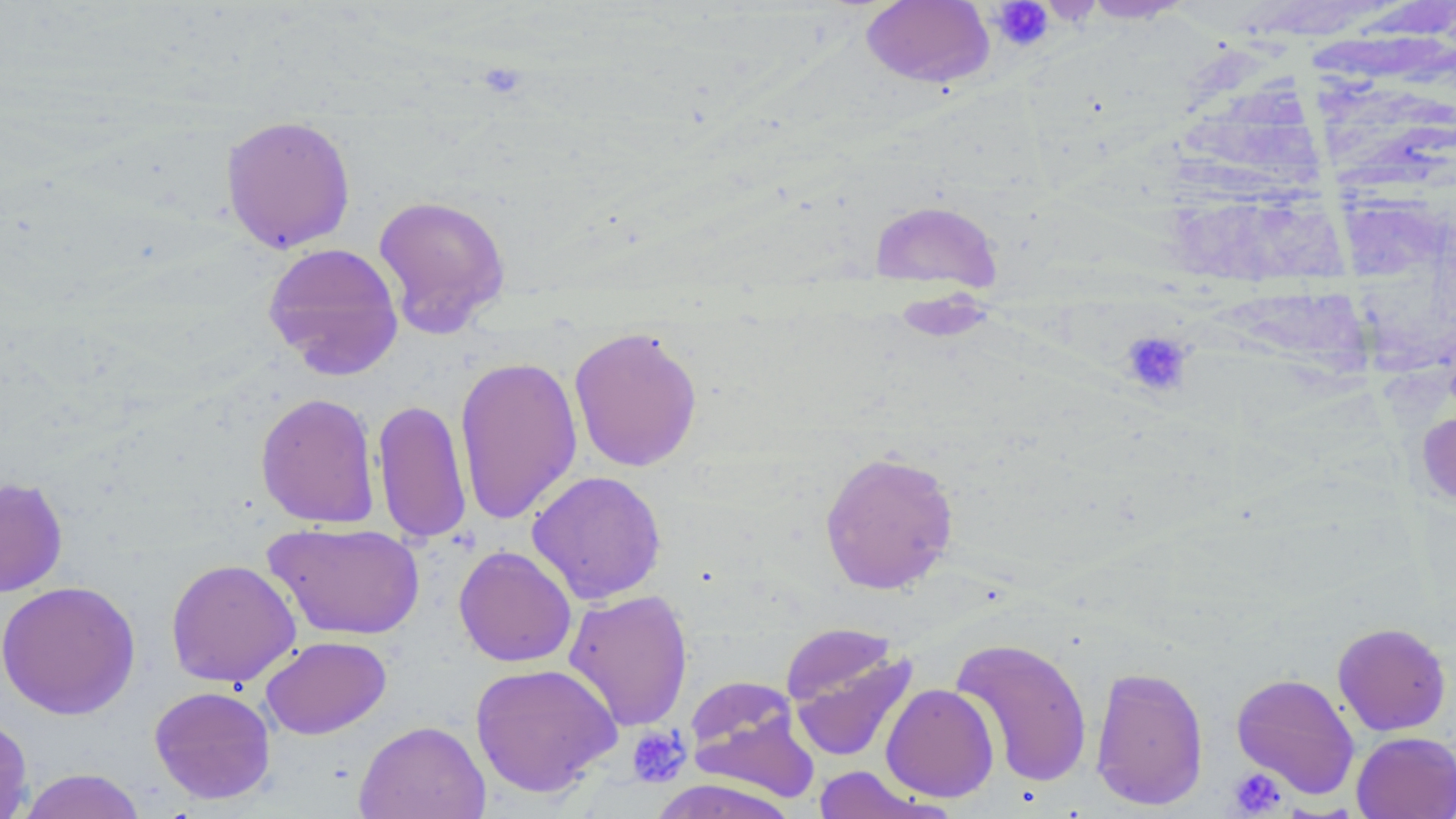 Approximate bounding boxes as [x1, y1, x2, y2] in pixels. Platelet locations: [990, 1, 1054, 52], [1120, 330, 1193, 398], [627, 725, 692, 786], [1228, 767, 1287, 817]. Uninfected red blood cell locations: [860, 0, 995, 89], [1077, 0, 1197, 24], [220, 114, 357, 254], [372, 194, 511, 336], [869, 199, 1004, 291], [1338, 210, 1456, 372], [262, 242, 404, 379], [568, 325, 704, 472], [454, 355, 582, 524], [255, 392, 380, 528], [373, 397, 472, 545], [819, 449, 959, 595], [526, 470, 667, 605], [0, 477, 68, 597], [264, 521, 426, 641], [453, 545, 577, 668], [166, 558, 301, 688], [0, 580, 141, 720], [563, 588, 694, 731], [780, 622, 902, 711], [1332, 622, 1452, 736], [260, 635, 392, 739], [950, 636, 1093, 788], [782, 638, 918, 766], [469, 662, 622, 799], [1089, 666, 1209, 810], [1231, 672, 1360, 799], [685, 678, 819, 802], [881, 683, 999, 802], [149, 685, 276, 804], [0, 713, 33, 819], [353, 719, 490, 819], [1351, 731, 1456, 819], [812, 766, 936, 819], [16, 768, 148, 819], [648, 778, 801, 819]. Slide-level diagnosis: negative for blood parasites. May-Grünwald-Giemsa-stained preparation. Captured at 1000x magnification. Optical microscopy. Thin blood film. Image is 1456×819 pixels. Single field of view.